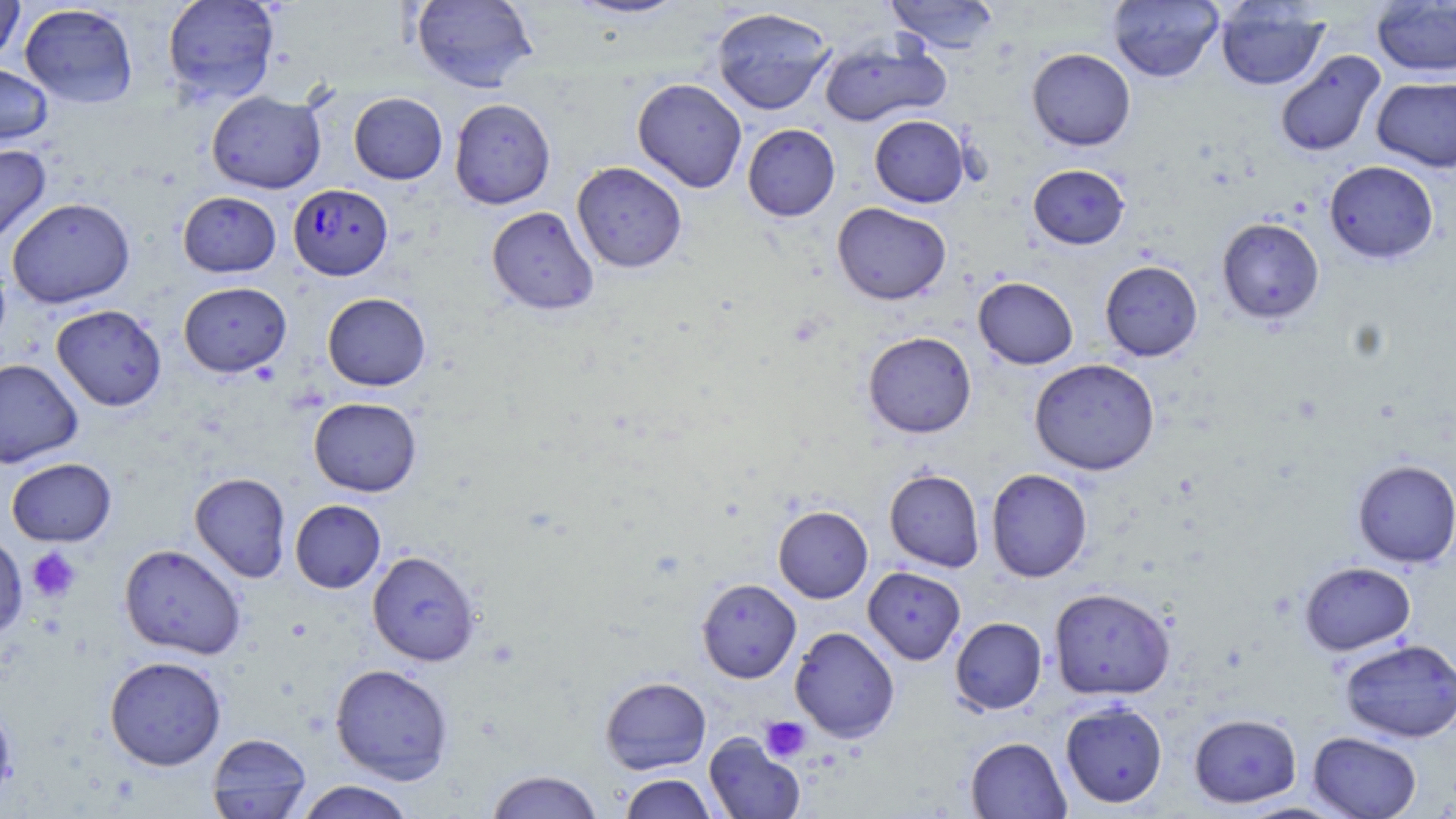

Summary:
  - Coordinate format: approximate bounding boxes as (x1, y1, x2, y2) in pixels
  - Plasmodium falciparum-infected red blood cell locations: (288, 183, 392, 280)
  - Platelet locations: (26, 546, 82, 602), (760, 716, 811, 762)
  - Uninfected red blood cell locations: (0, 0, 24, 64), (162, 0, 280, 104), (411, 0, 538, 93), (565, 0, 690, 20), (885, 0, 1000, 53), (1108, 0, 1223, 83), (1371, 0, 1456, 77), (1215, 2, 1329, 91), (19, 3, 138, 108), (711, 7, 835, 115), (819, 36, 950, 128), (1027, 48, 1136, 151), (1274, 50, 1386, 158), (0, 62, 53, 149), (1372, 76, 1456, 172), (632, 78, 747, 193), (206, 90, 326, 194), (348, 92, 447, 184), (449, 97, 556, 209), (869, 115, 970, 207), (742, 124, 840, 221), (0, 143, 51, 247), (1324, 161, 1438, 264), (571, 162, 687, 273), (1028, 164, 1130, 249), (178, 191, 281, 277), (7, 197, 135, 308), (832, 202, 951, 304), (487, 206, 599, 315), (1217, 217, 1324, 324), (1099, 260, 1203, 361), (973, 276, 1078, 369), (178, 281, 291, 377), (322, 292, 431, 391), (51, 304, 166, 411), (863, 331, 977, 437), (0, 358, 83, 468), (1029, 358, 1160, 476), (309, 397, 422, 496), (6, 457, 117, 546), (1352, 459, 1456, 568), (884, 468, 985, 572), (986, 468, 1093, 582), (189, 472, 291, 582), (290, 499, 386, 593), (773, 505, 873, 603), (0, 533, 27, 641), (119, 543, 246, 660), (367, 550, 481, 666), (1299, 561, 1416, 655), (863, 566, 966, 665), (696, 578, 801, 683), (1048, 587, 1175, 700), (950, 617, 1047, 714), (789, 626, 900, 742), (1339, 638, 1456, 743), (104, 655, 227, 770), (330, 663, 454, 784), (600, 676, 711, 774), (1060, 700, 1168, 808), (1188, 712, 1301, 808), (1308, 731, 1422, 818), (206, 732, 312, 818), (704, 733, 805, 818), (965, 736, 1071, 819), (485, 770, 604, 818), (619, 773, 718, 818), (293, 780, 416, 819), (1236, 801, 1350, 818)
  - Slide-level diagnosis: Plasmodium falciparum
  - Preparation: thin blood smear
  - Image size: 1456×819 pixels
  - Modality: light microscopy
  - Magnification: 1000x
  - Field of view: single
  - Stain: May-Grünwald-Giemsa